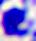

identification: white blood cell
magnification: 400x
modality: micrograph